Assess the morphology of the erythrocytes.
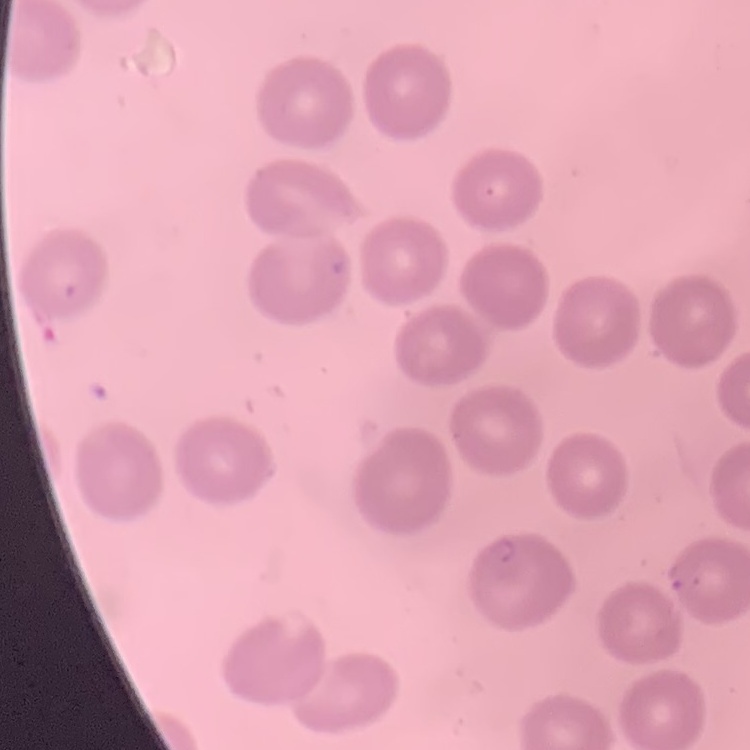
No rouleaux formation.

Summary:
  - Stain: Field's or Giemsa
  - Image type: square crop of a larger photomicrograph
  - Preparation: thin blood smear